Give the preparation type.
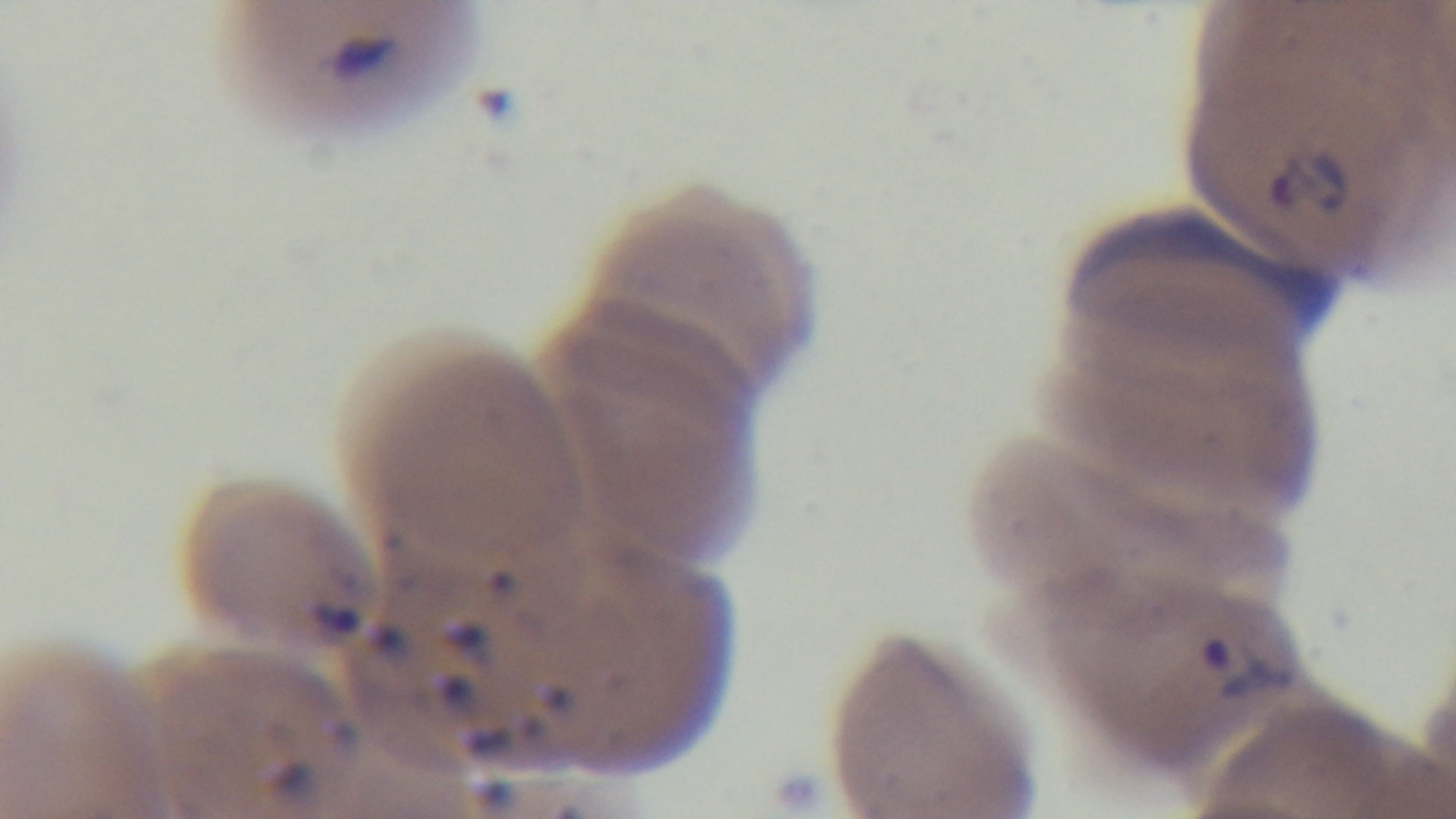

A thin smear.

field_of_view: single
modality: light microscopy
objective: 100x oil immersion
stain: Giemsa
capture: mounted 4K digital camera
malaria_status: infected